Name the parasite shown.
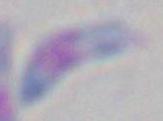
This is Toxoplasma gondii.

modality: photomicrograph
magnification: 1000x